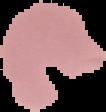

Image is 106×112 pixels. Malaria status: parasitized. The area outside the segmented cell region is set to black. From a thin blood film.